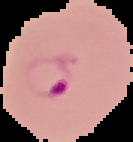

Summary:
  - Image type: segmented cell region on a black background
  - Image size: 133×142 pixels
  - Result: malaria parasites identified
  - Preparation: thin blood smear